State the blood parasite species.
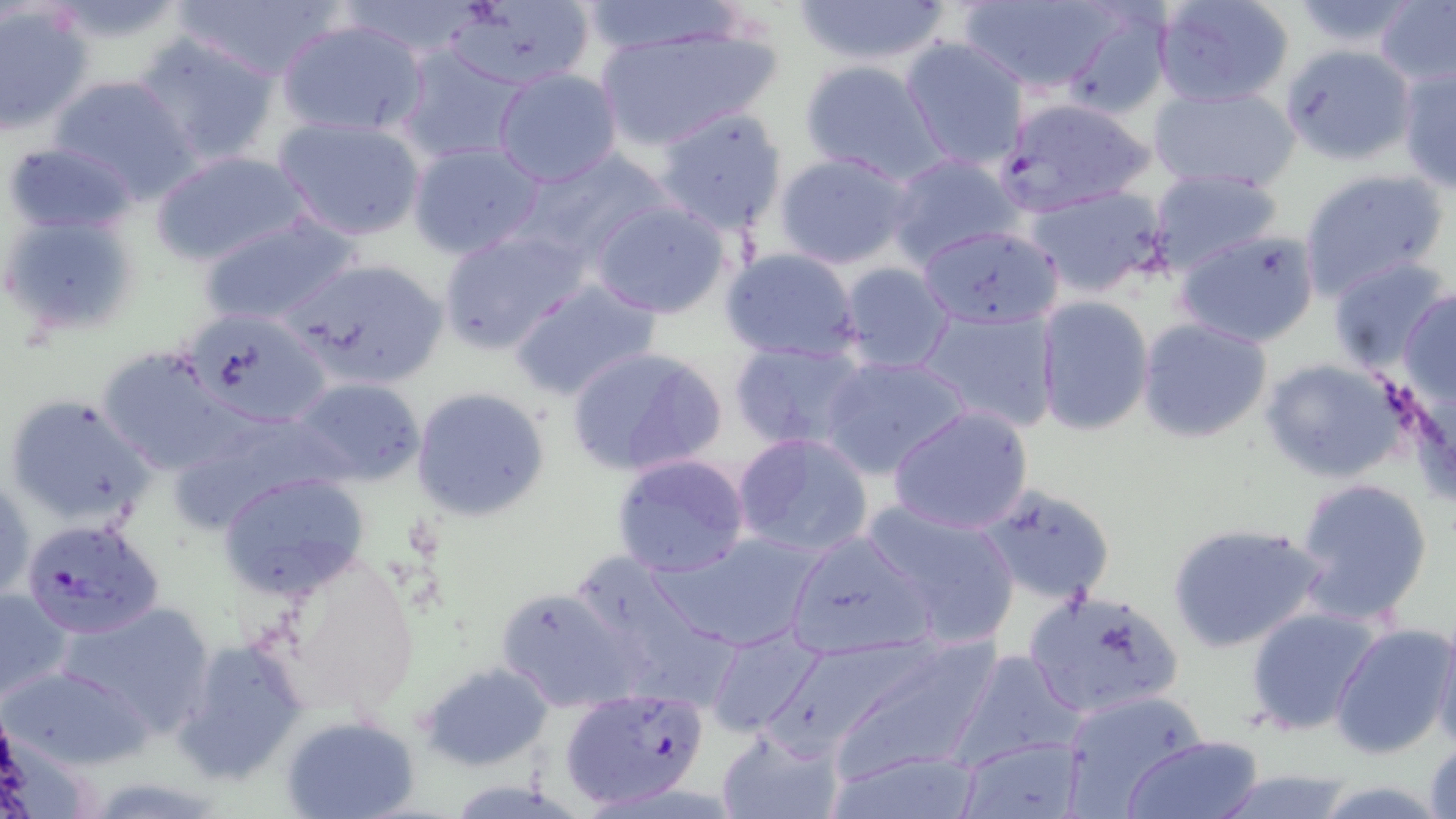

Plasmodium falciparum.

Approximate bounding boxes as (x1,y1)-(x2,y2) corner pairs in pixels. Plasmodium falciparum-infected red blood cell locations: (995,96)-(1155,216), (20,517)-(167,640), (559,686)-(712,811). Uninfected red blood cell locations: (169,0)-(345,81), (336,0)-(488,62), (447,0)-(598,91), (788,0)-(956,69), (1152,0)-(1296,108), (1377,0)-(1456,89), (571,1)-(745,56), (952,1)-(1126,93), (1290,1)-(1422,52), (0,5)-(94,134), (1056,6)-(1173,123), (275,15)-(429,139), (593,21)-(780,152), (134,30)-(279,167), (900,37)-(1030,170), (1280,44)-(1415,166), (395,45)-(528,167), (798,59)-(944,182), (1397,59)-(1455,194), (492,68)-(623,187), (47,74)-(199,203), (1149,85)-(1301,194), (653,105)-(789,235), (273,116)-(427,243), (1,139)-(144,236), (406,139)-(546,260), (511,147)-(670,267), (149,150)-(312,269), (774,151)-(917,270), (885,153)-(1021,269), (1146,168)-(1284,277), (1298,170)-(1451,300), (1023,185)-(1173,299), (587,198)-(736,319), (2,210)-(140,337), (198,214)-(360,331), (437,224)-(587,353), (917,224)-(1065,329), (1175,228)-(1322,349), (721,246)-(863,364), (279,256)-(451,392), (1327,257)-(1453,376), (838,262)-(956,375), (510,278)-(663,402), (1399,289)-(1456,407), (1032,296)-(1155,435), (915,305)-(1061,433), (178,307)-(334,426), (1136,316)-(1274,445), (730,338)-(871,456), (565,343)-(728,479), (96,345)-(241,475), (819,353)-(974,479), (1260,359)-(1404,484), (287,376)-(427,485), (411,385)-(552,522), (5,392)-(154,530), (165,403)-(344,535), (887,404)-(1034,535), (732,432)-(875,561), (610,453)-(752,577), (217,471)-(371,599), (1,473)-(33,606), (1293,477)-(1434,625), (975,484)-(1118,605), (860,499)-(1022,647), (1165,521)-(1328,654), (785,527)-(940,657), (649,530)-(827,654), (263,553)-(422,721), (0,583)-(77,709), (495,586)-(642,711), (1025,589)-(1187,720), (50,599)-(215,737), (1243,607)-(1387,736), (1429,620)-(1456,753), (1330,623)-(1453,758), (701,624)-(824,741), (819,636)-(1000,786), (174,637)-(310,784), (950,649)-(1088,767), (420,661)-(554,769), (3,662)-(155,771), (1059,689)-(1209,815), (281,715)-(419,819), (717,728)-(843,819), (955,734)-(1087,819), (1119,734)-(1266,819), (1424,737)-(1456,818), (827,747)-(983,819), (1211,767)-(1359,819). Image is 1456×819 pixels. 1000x magnification. Light microscopy. May-Grünwald-Giemsa-stained preparation. Single field of view. Thin blood smear.